Identify the parasite.
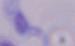
A trypanosome.

1000x magnification. Micrograph.